State which cell type is depicted.
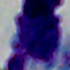

A leukocyte.

Photomicrograph. 1000x magnification.